Report the malaria status of this cell.
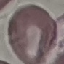

It is uninfected.

stain = Giemsa
preparation = thin blood film
capture = smartphone camera at the microscope eyepiece
image type = cell patch, automatically extracted from a larger field of view and resized to 64 × 64 pixels